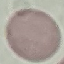

malaria_status: uninfected
capture: smartphone through the microscope eyepiece
image_type: automatically extracted cell patch, resized to 64 × 64 pixels
preparation: thin smear
stain: Giemsa